Describe the morphology of the erythrocytes.
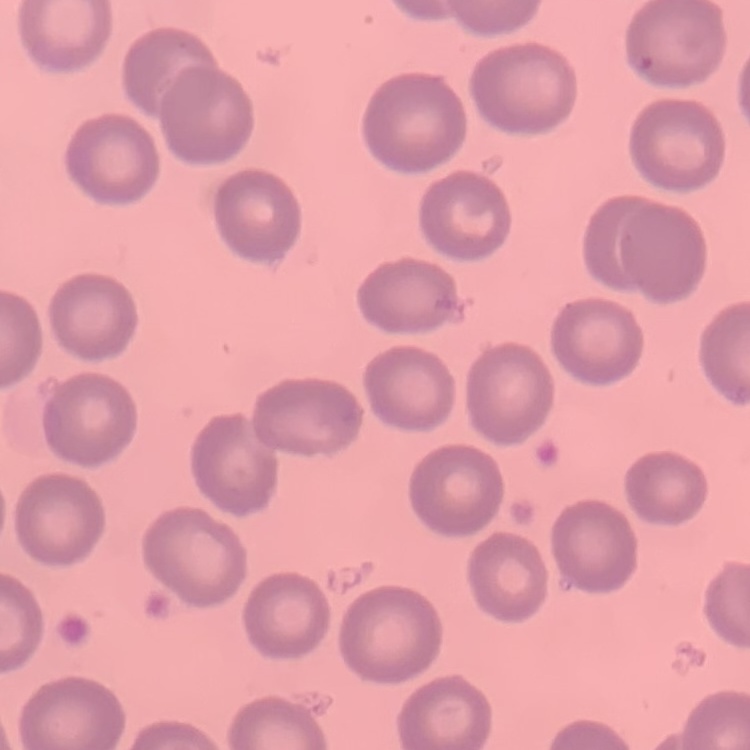
No rouleaux formation.

{
  "image_type": "one tile cut from a larger photomicrograph",
  "stain": "Field's or Giemsa",
  "preparation": "thin peripheral smear"
}